Assess this cell for malaria.
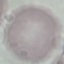

It is uninfected.

preparation = thin blood smear
stain = Giemsa
image type = automatically extracted cell patch, resized to 64 × 64 pixels
capture = smartphone through the microscope eyepiece